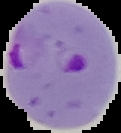

preparation = thin blood smear
image size = 121×133 pixels
malaria status = parasitized
image type = segmented cell region with the area outside set to black